Assess the background quality.
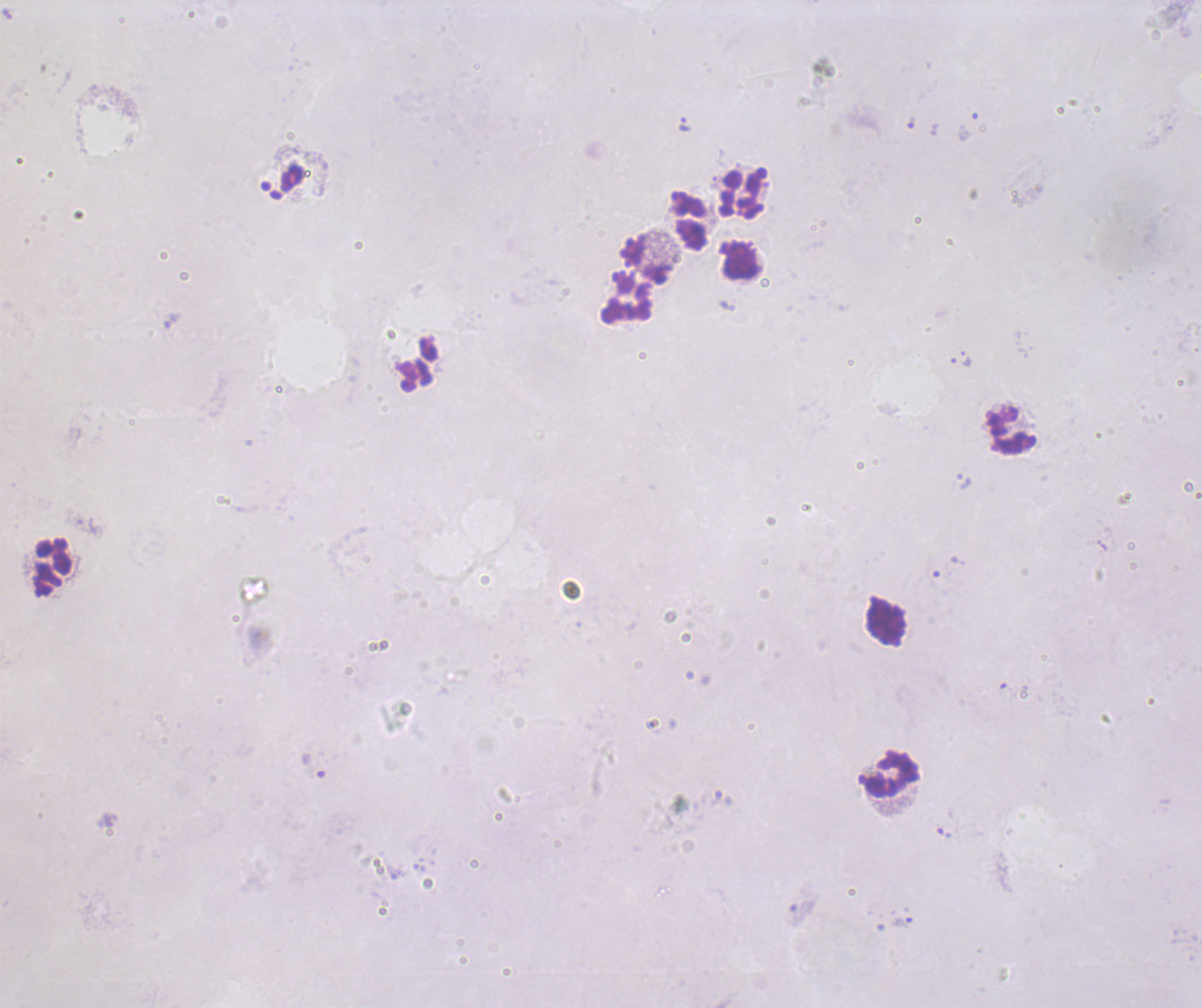
It is poor.

Approximate centers as (x, y) in pixels. Leukocyte locations: (741, 194), (690, 219), (739, 260), (647, 261), (626, 297), (1012, 429), (53, 568), (886, 622), (892, 774). Trophozoite locations: (684, 124), (965, 359), (902, 921). Thick blood smear. Romanowsky stain. Image is 1202×1008 pixels. Result: positive for malaria parasites. Coloration quality: bad. One field from this slide. 100x magnification. Previously used in an actual diagnosis.